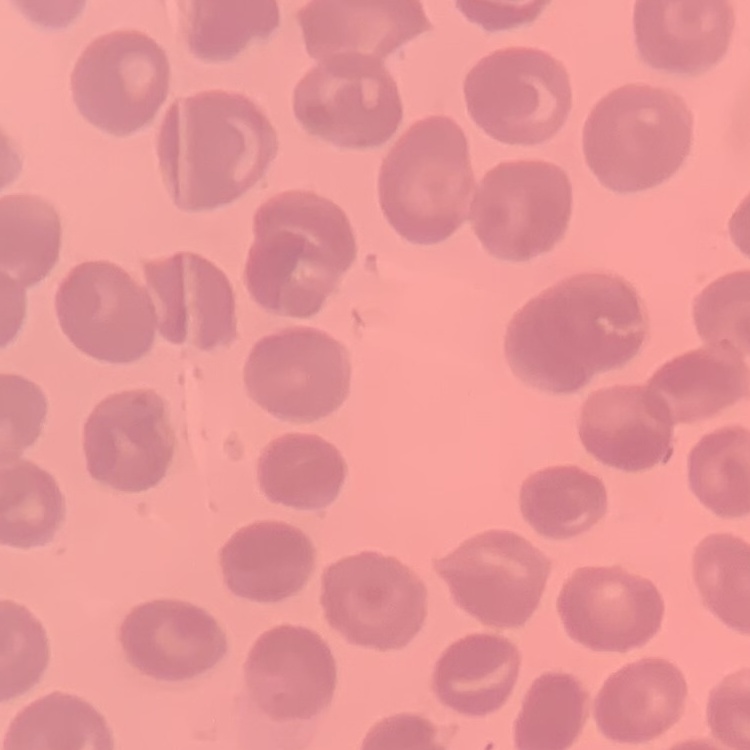 The red blood cells show no rouleaux formation. Stained with either Field's or Giemsa. Thin blood smear. One tile cut from a larger photomicrograph.